State the preparation type.
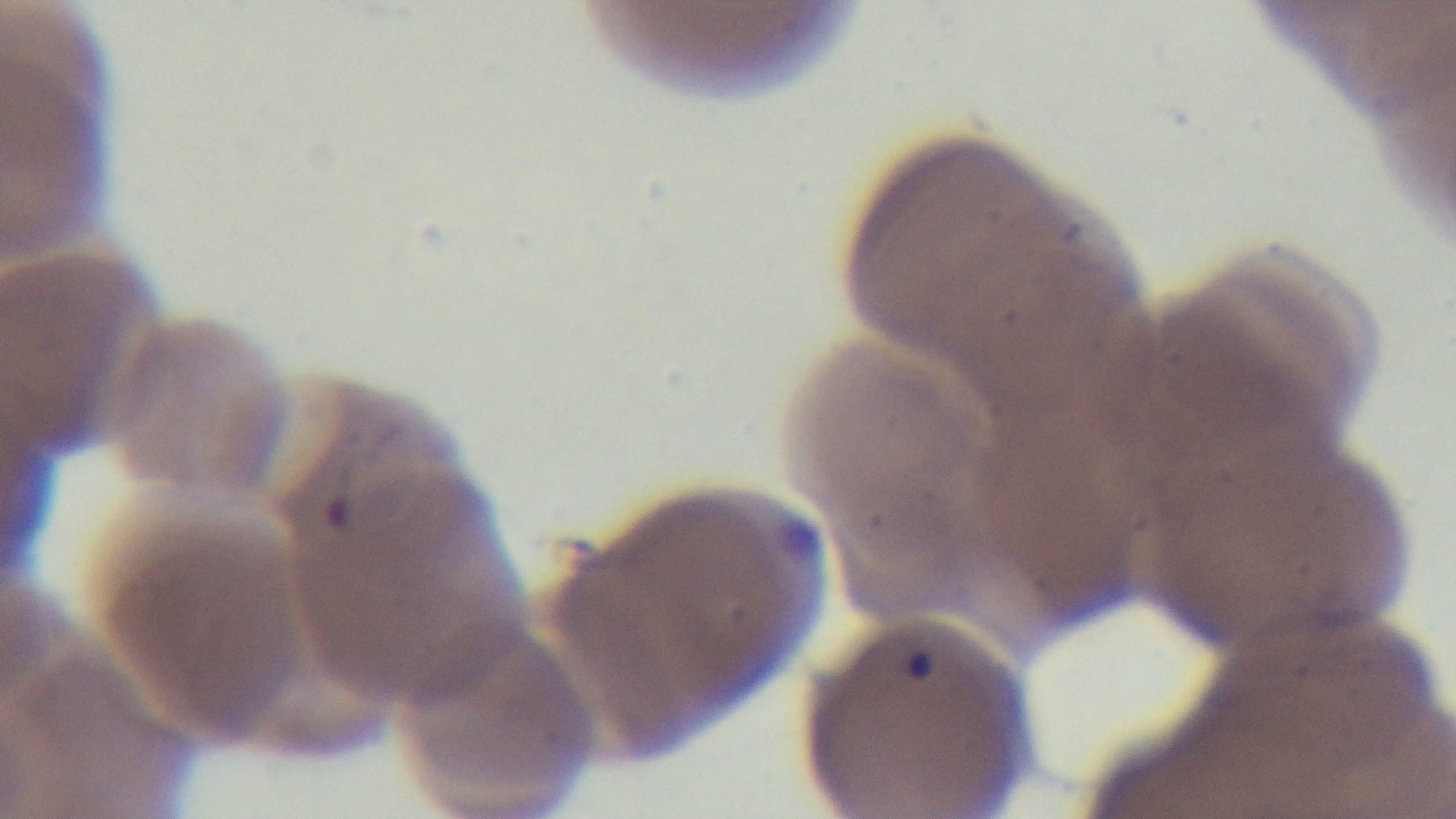

It is a thin blood film.

Malaria status: positive. Oil-immersion objective, 100x. Mounted 4K digital camera. One field from the slide. Photomicrograph. Giemsa stain.